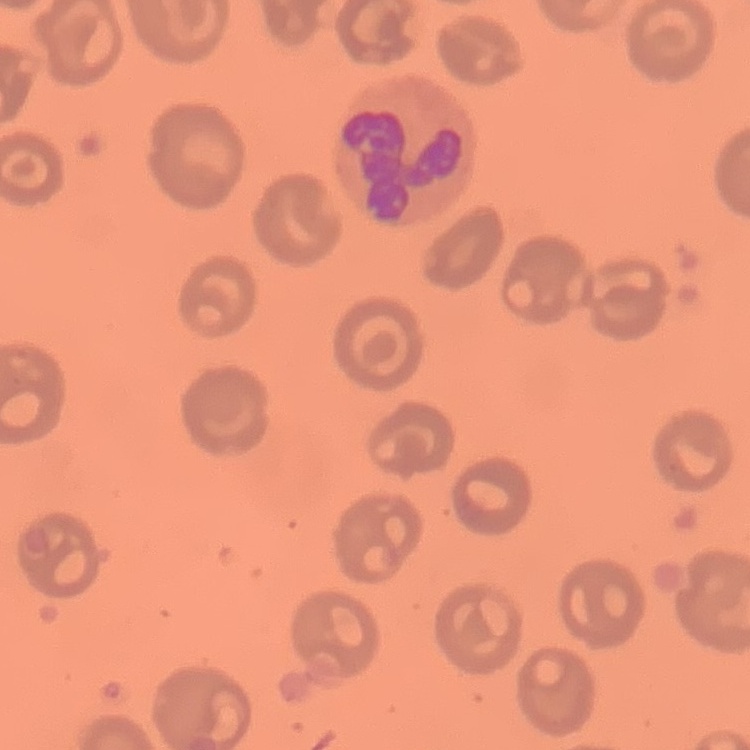

Summary:
  - Erythrocyte morphology: no rouleaux formation
  - Stain: Field's or Giemsa
  - Image type: one tile cut from a larger photomicrograph
  - Preparation: thin blood film